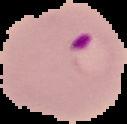

Summary:
  - Image type: segmented cell region on a black background
  - Result: Plasmodium parasites identified
  - Image size: 127×124 pixels
  - Preparation: thin blood smear